Assess this cell for malaria.
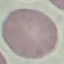
It is uninfected.

Summary:
  - Stain: Giemsa
  - Image type: automatically extracted cell patch, resized to 64 × 64 pixels
  - Capture: smartphone through the microscope eyepiece
  - Preparation: thin blood smear